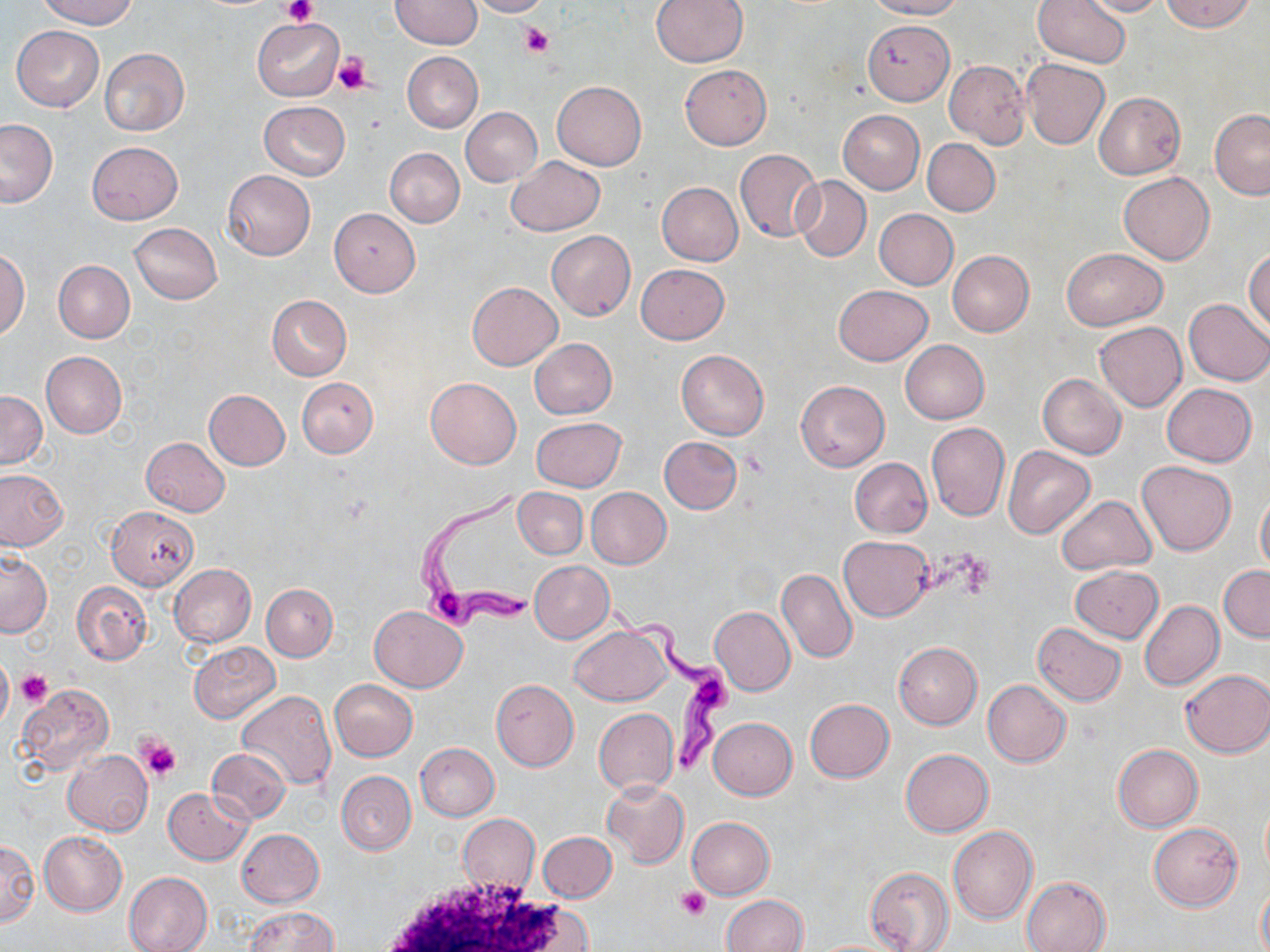
Summary:
  - Coordinate format: approximate bounding boxes as named x1/y1/x2/y2 corners in pixels
  - White blood cell locations: (x1=368, y1=873, x2=590, y2=952)
  - Trypanosoma brucei locations: (x1=409, y1=479, x2=540, y2=631), (x1=607, y1=604, x2=738, y2=774)
  - Uninfected red blood cell locations: (x1=38, y1=0, x2=139, y2=28), (x1=466, y1=0, x2=549, y2=17), (x1=651, y1=0, x2=747, y2=67), (x1=866, y1=0, x2=963, y2=20), (x1=1032, y1=0, x2=1131, y2=68), (x1=1077, y1=0, x2=1167, y2=18), (x1=1162, y1=0, x2=1255, y2=33), (x1=391, y1=1, x2=482, y2=50), (x1=251, y1=18, x2=343, y2=101), (x1=863, y1=19, x2=954, y2=103), (x1=512, y1=22, x2=556, y2=59), (x1=12, y1=26, x2=104, y2=111), (x1=100, y1=48, x2=190, y2=136), (x1=402, y1=51, x2=482, y2=132), (x1=1021, y1=58, x2=1110, y2=149), (x1=944, y1=61, x2=1030, y2=148), (x1=680, y1=64, x2=771, y2=149), (x1=552, y1=80, x2=647, y2=169), (x1=1094, y1=91, x2=1185, y2=180), (x1=259, y1=102, x2=350, y2=179), (x1=461, y1=107, x2=541, y2=186), (x1=1210, y1=109, x2=1270, y2=199), (x1=837, y1=110, x2=925, y2=193), (x1=0, y1=118, x2=56, y2=207), (x1=923, y1=139, x2=1000, y2=216), (x1=87, y1=141, x2=182, y2=224), (x1=385, y1=148, x2=463, y2=227), (x1=734, y1=148, x2=824, y2=242), (x1=505, y1=156, x2=605, y2=236), (x1=223, y1=171, x2=316, y2=260), (x1=1117, y1=172, x2=1215, y2=265), (x1=792, y1=176, x2=871, y2=261), (x1=656, y1=182, x2=743, y2=267), (x1=331, y1=208, x2=420, y2=296), (x1=874, y1=209, x2=958, y2=290), (x1=130, y1=223, x2=222, y2=304), (x1=547, y1=230, x2=635, y2=320), (x1=1245, y1=246, x2=1269, y2=334), (x1=1061, y1=247, x2=1167, y2=330), (x1=946, y1=249, x2=1034, y2=336), (x1=0, y1=250, x2=28, y2=339), (x1=53, y1=260, x2=134, y2=343), (x1=636, y1=263, x2=729, y2=344), (x1=467, y1=282, x2=562, y2=369), (x1=834, y1=285, x2=932, y2=365), (x1=267, y1=295, x2=351, y2=380), (x1=1183, y1=298, x2=1270, y2=386), (x1=1094, y1=322, x2=1186, y2=411), (x1=530, y1=338, x2=616, y2=419), (x1=899, y1=340, x2=989, y2=425), (x1=676, y1=349, x2=769, y2=440), (x1=41, y1=351, x2=126, y2=437), (x1=1038, y1=374, x2=1126, y2=459), (x1=297, y1=377, x2=378, y2=457), (x1=425, y1=377, x2=522, y2=469), (x1=796, y1=380, x2=889, y2=471), (x1=1162, y1=383, x2=1257, y2=466), (x1=203, y1=389, x2=290, y2=470), (x1=0, y1=392, x2=47, y2=468), (x1=531, y1=417, x2=626, y2=491), (x1=925, y1=421, x2=1009, y2=521), (x1=659, y1=436, x2=742, y2=514), (x1=140, y1=437, x2=231, y2=516), (x1=1003, y1=446, x2=1095, y2=538), (x1=850, y1=458, x2=932, y2=537), (x1=1137, y1=460, x2=1235, y2=555), (x1=0, y1=470, x2=66, y2=550), (x1=1256, y1=486, x2=1270, y2=574), (x1=514, y1=487, x2=587, y2=559), (x1=586, y1=487, x2=671, y2=568), (x1=1055, y1=495, x2=1156, y2=575), (x1=106, y1=505, x2=199, y2=590), (x1=838, y1=534, x2=934, y2=621), (x1=0, y1=552, x2=52, y2=637), (x1=529, y1=560, x2=614, y2=642), (x1=169, y1=563, x2=256, y2=647), (x1=1069, y1=564, x2=1164, y2=642), (x1=1219, y1=565, x2=1270, y2=641), (x1=776, y1=568, x2=857, y2=663), (x1=73, y1=581, x2=151, y2=665), (x1=262, y1=583, x2=337, y2=661), (x1=1139, y1=600, x2=1223, y2=690), (x1=369, y1=605, x2=466, y2=692), (x1=709, y1=606, x2=795, y2=696), (x1=1033, y1=622, x2=1127, y2=706), (x1=570, y1=623, x2=673, y2=706), (x1=188, y1=641, x2=280, y2=723), (x1=894, y1=642, x2=982, y2=729), (x1=0, y1=652, x2=13, y2=731), (x1=1181, y1=669, x2=1270, y2=758), (x1=329, y1=679, x2=418, y2=760), (x1=491, y1=679, x2=578, y2=770), (x1=982, y1=680, x2=1071, y2=767), (x1=19, y1=684, x2=115, y2=774), (x1=236, y1=690, x2=337, y2=791), (x1=805, y1=699, x2=894, y2=782), (x1=594, y1=707, x2=679, y2=795), (x1=708, y1=717, x2=797, y2=799), (x1=415, y1=743, x2=498, y2=820), (x1=1112, y1=744, x2=1204, y2=832), (x1=206, y1=748, x2=291, y2=823), (x1=900, y1=748, x2=994, y2=838), (x1=63, y1=751, x2=152, y2=835), (x1=337, y1=771, x2=415, y2=854), (x1=603, y1=781, x2=688, y2=867), (x1=164, y1=786, x2=252, y2=864), (x1=458, y1=815, x2=539, y2=894), (x1=687, y1=817, x2=773, y2=899), (x1=1150, y1=822, x2=1242, y2=910), (x1=948, y1=827, x2=1038, y2=924), (x1=237, y1=829, x2=324, y2=906), (x1=39, y1=830, x2=127, y2=915), (x1=537, y1=832, x2=617, y2=903), (x1=0, y1=839, x2=40, y2=927), (x1=865, y1=865, x2=954, y2=952), (x1=124, y1=872, x2=213, y2=952), (x1=1021, y1=876, x2=1111, y2=952), (x1=1257, y1=881, x2=1270, y2=952), (x1=722, y1=894, x2=808, y2=952), (x1=242, y1=907, x2=339, y2=952)
  - Platelet locations: (x1=284, y1=0, x2=316, y2=25), (x1=519, y1=24, x2=554, y2=57), (x1=333, y1=52, x2=372, y2=95), (x1=17, y1=670, x2=52, y2=707), (x1=136, y1=735, x2=182, y2=782), (x1=677, y1=886, x2=712, y2=918)
  - Slide-level diagnosis: Trypanosoma brucei
  - Field of view: single
  - Preparation: thin blood film
  - Magnification: 1000x
  - Image size: 1270×952 pixels
  - Modality: light microscopy
  - Stain: May-Grünwald-Giemsa